Comment on the morphology of the red blood cells.
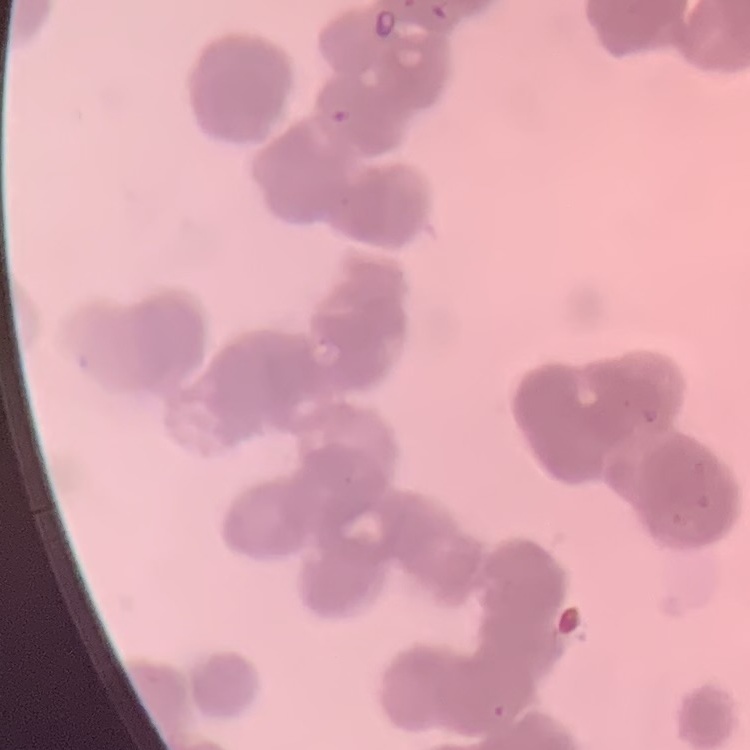

Rouleaux formation.

Field's or Giemsa stain. One tile cut from a larger photomicrograph. Thin blood smear.